Comment on the morphology of the erythrocytes.
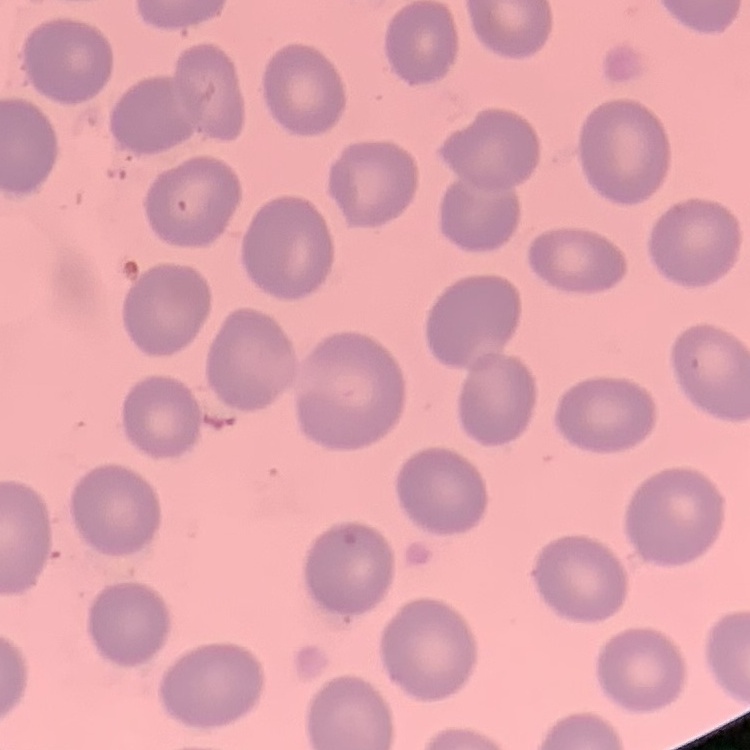
They show no rouleaux formation.

image type = one tile cut from a larger photomicrograph
preparation = thin peripheral smear
stain = Field's or Giemsa